Assess this cell for malaria.
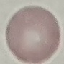

Uninfected.

Automatically extracted cell patch, resized to 64 × 64 pixels. Thin smear of blood. Giemsa stain. Photographed with a smartphone camera at the microscope eyepiece.